Look for Plasmodium parasites.
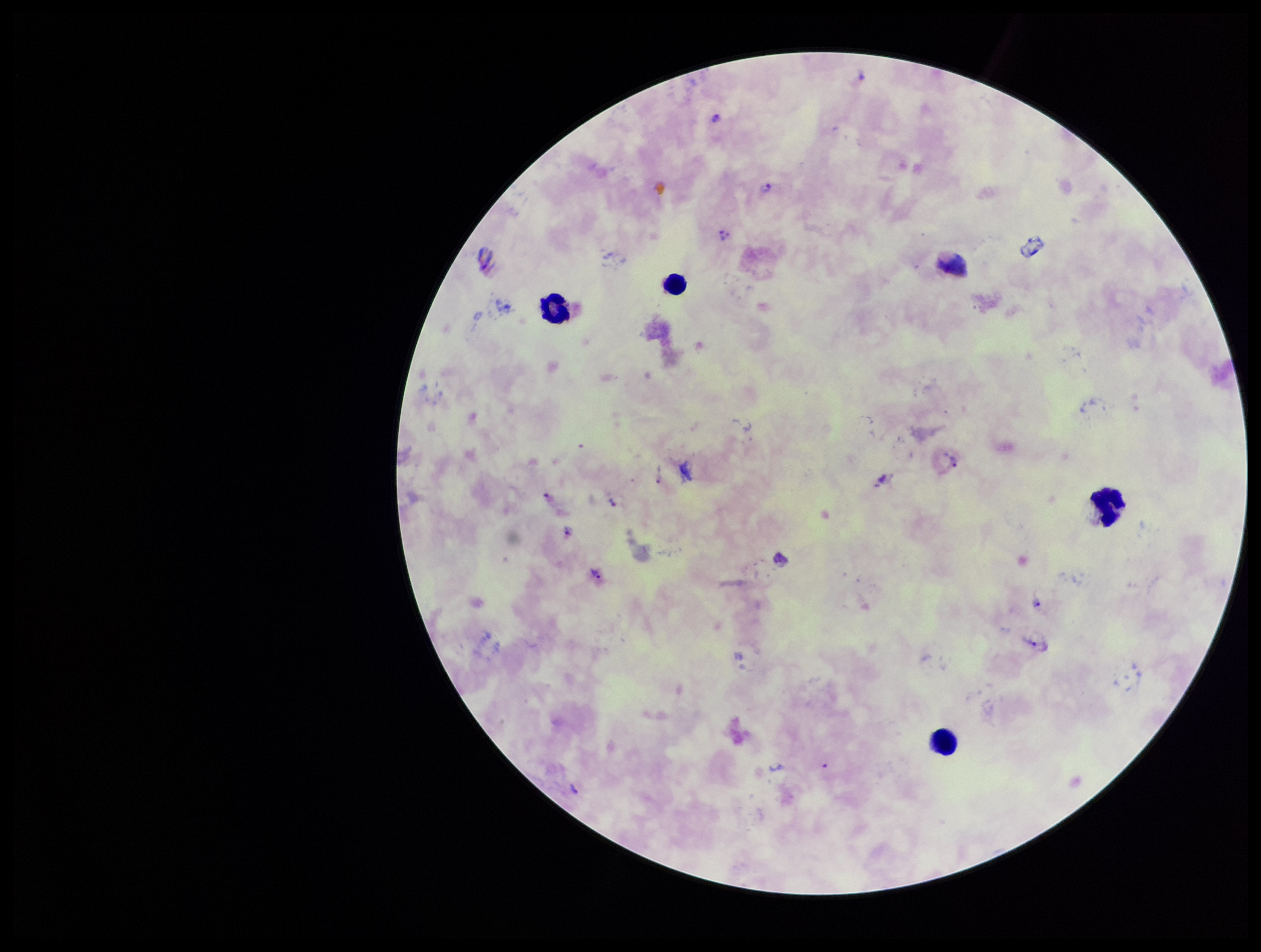
Detected.

species reported for this patient = Plasmodium vivax
leukocyte count = 5
parasite count = 8
field of view = single
image size = 1261×952 pixels
stain = Giemsa
capture = smartphone photograph through the microscope eyepiece
preparation = thick blood smear
patient malaria status = positive